Identify the parasite.
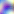
This is Toxoplasma gondii.

Summary:
  - Magnification: 400x
  - Modality: photomicrograph